Classify this cell by malaria status.
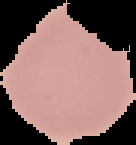

Uninfected.

Summary:
  - Image type: segmented cell region on a black background
  - Preparation: thin blood film
  - Image size: 136×145 pixels